State which cell type is depicted.
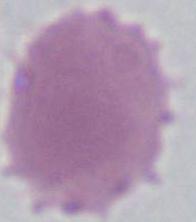
An erythrocyte.

1000x magnification. Photomicrograph.